Describe the morphology of the erythrocytes.
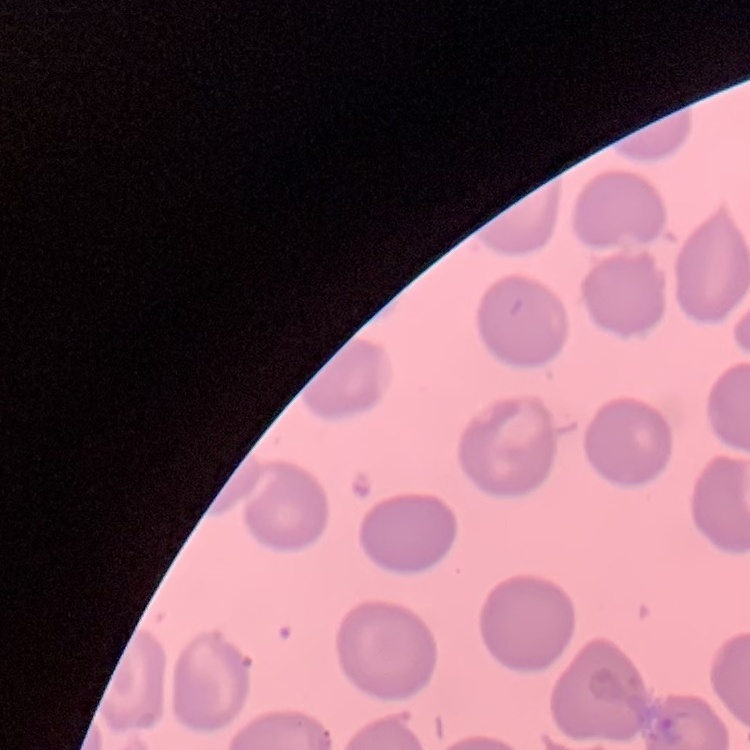

No rouleaux formation.

Summary:
  - Preparation: thin blood film
  - Stain: Field's or Giemsa
  - Image type: square crop of a larger photomicrograph